Comment on the morphology of the erythrocytes.
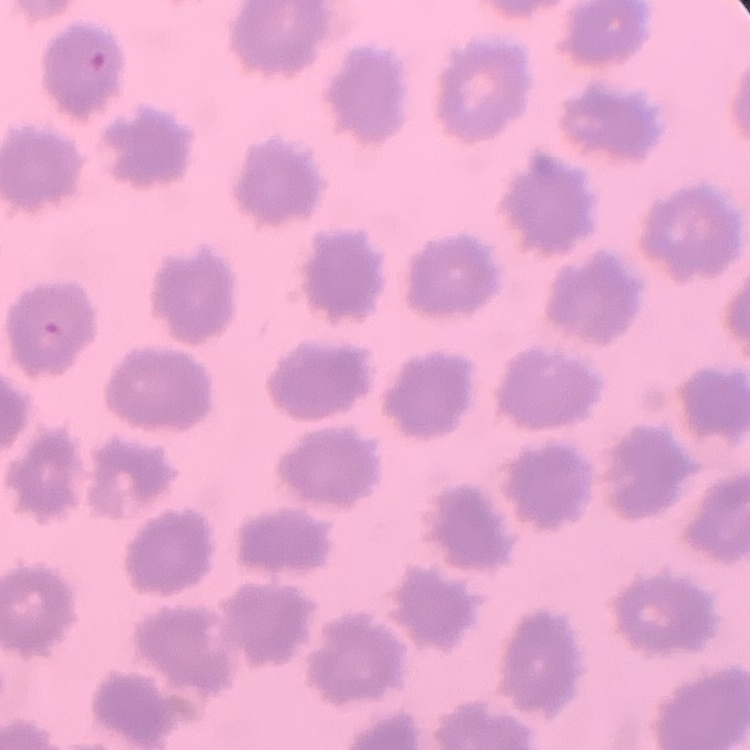

No rouleaux formation.

image type = one tile cut from a larger photomicrograph
preparation = thin peripheral smear
stain = Field's or Giemsa